Report the malaria status of this cell.
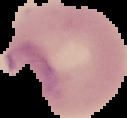
Parasitized.

Summary:
  - Preparation: thin blood smear
  - Image type: cell region segmented out of the field of view; surrounding area masked to black
  - Image size: 127×118 pixels